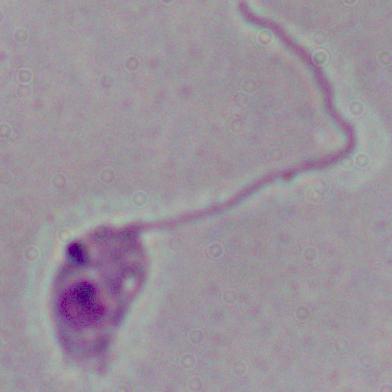

magnification: 1000x
modality: micrograph
identification: Leishmania